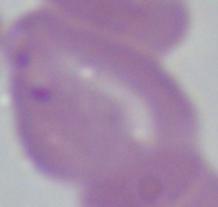

{
  "magnification": "1000x",
  "identification": "Babesia",
  "modality": "micrograph"
}